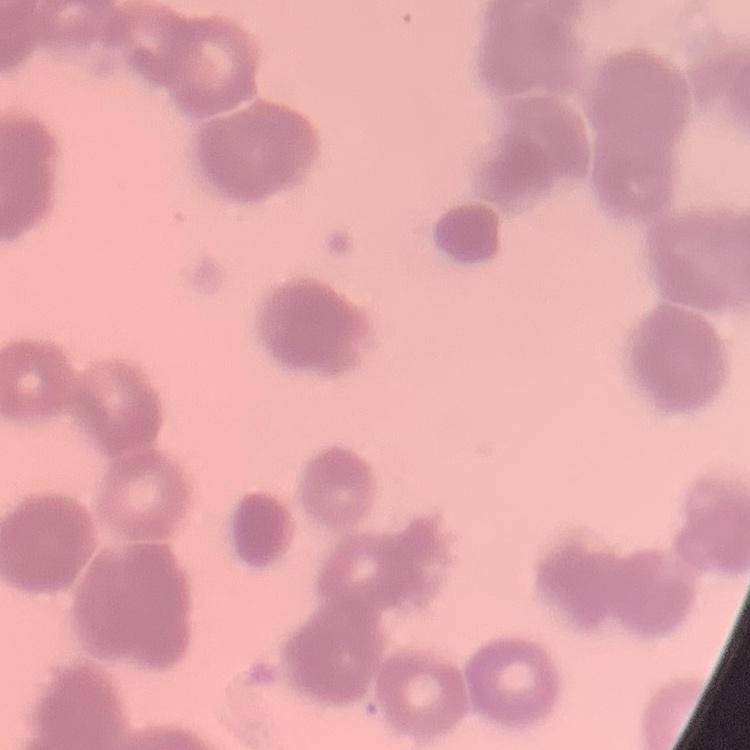
Summary:
  - Red blood cell morphology: rouleaux formation
  - Stain: Field's or Giemsa
  - Image type: one tile cut from a larger photomicrograph
  - Preparation: thin blood film